Identify the preparation type.
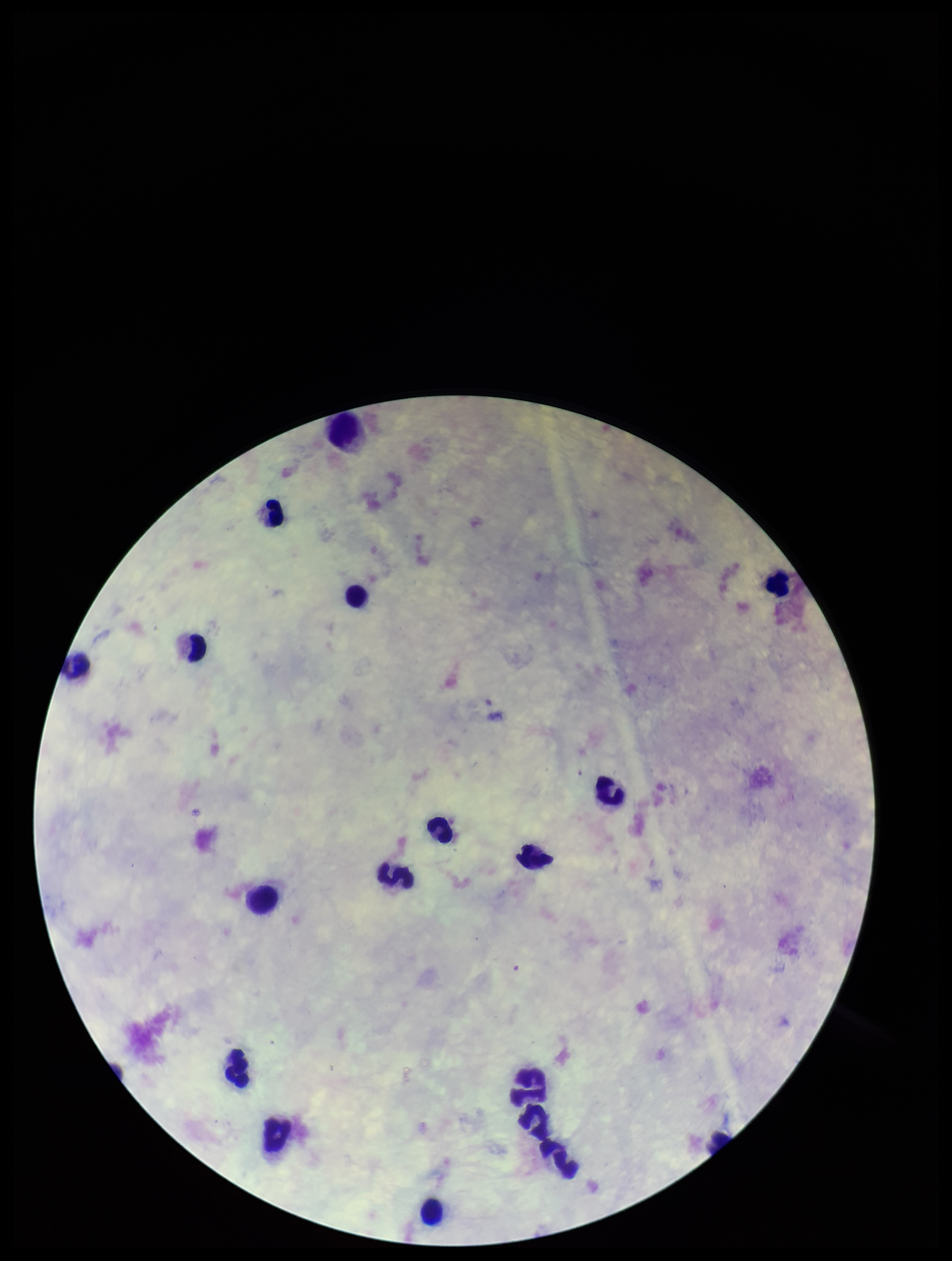

Thick.

Summary:
  - Patient malaria status: negative
  - Leukocyte count: 18
  - Capture: smartphone photograph through the microscope eyepiece
  - Parasite count: 0
  - Stain: Giemsa
  - Image size: 952×1261 pixels
  - Field of view: single
  - Plasmodium parasites: none seen